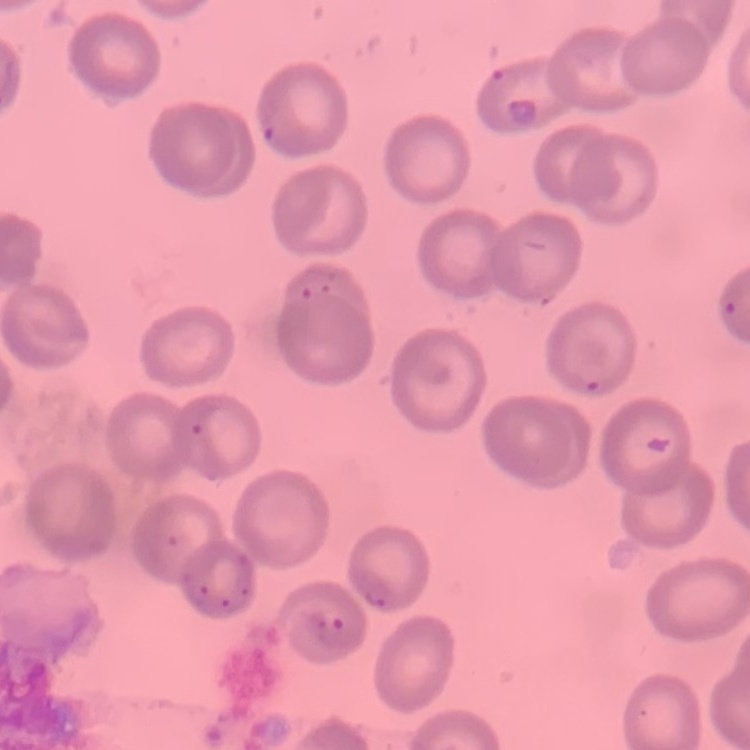

red_blood_cell_morphology: no rouleaux formation
preparation: thin blood smear
stain: Field's or Giemsa
image_type: one tile cut from a larger photomicrograph